Give the position of every P. falciparum parasite, noting its life-cycle stage.
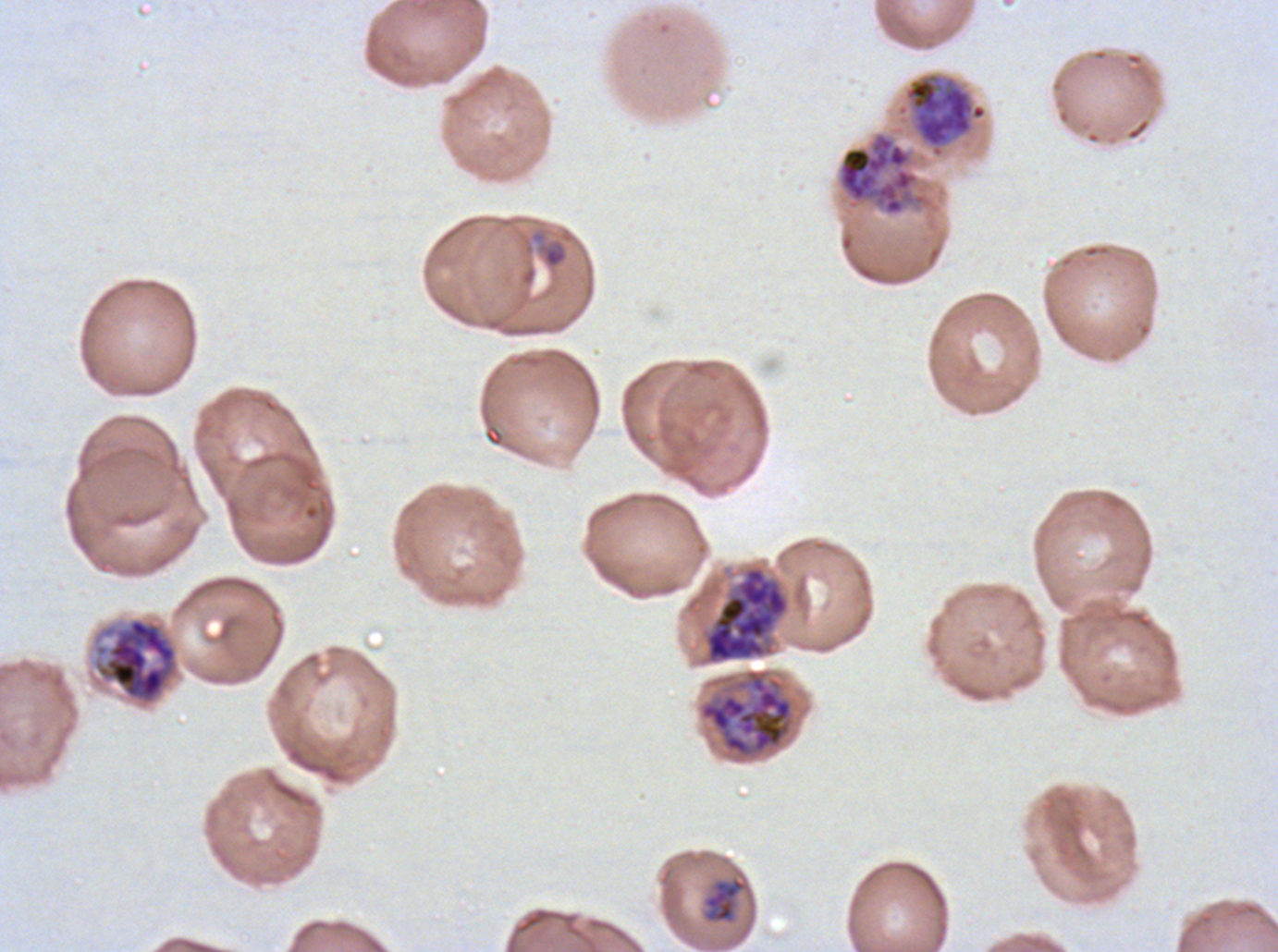
Approximate bounding boxes as [x1, y1, x2, y2] in pixels.
Late-ring/early-trophozoite forms: [543, 245, 567, 268].
Late trophozoites: [704, 877, 746, 922].
Early schizonts: [903, 71, 988, 158], [704, 566, 790, 665], [92, 616, 180, 707], [697, 667, 796, 762].
No rings, mid trophozoites, late schizonts, segmenters, or gametocytes observed.

Thin blood film. A sub-image separated from a larger composite. Image is 1278×952 pixels. P. falciparum cultured ex vivo for 24 to 48 hours, from a patient in The Gambia. Giemsa stain. Life-cycle stages observed: late-ring/early-trophozoite, late trophozoite, early schizont.